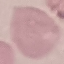
Result: no malaria parasites detected. Thin blood smear. Acquired by smartphone through the microscope eyepiece. Cell patch, automatically extracted from a larger field of view and resized to 64 × 64 pixels. Giemsa stain.